Name the parasite shown.
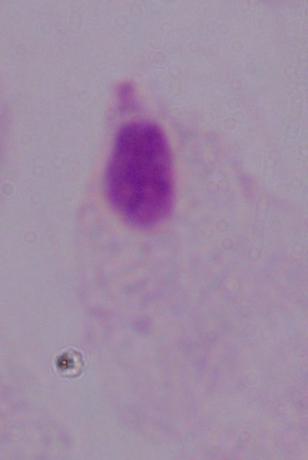
This is a trichomonad.

Summary:
  - Magnification: 1000x
  - Modality: micrograph